Point out each Plasmodium parasite.
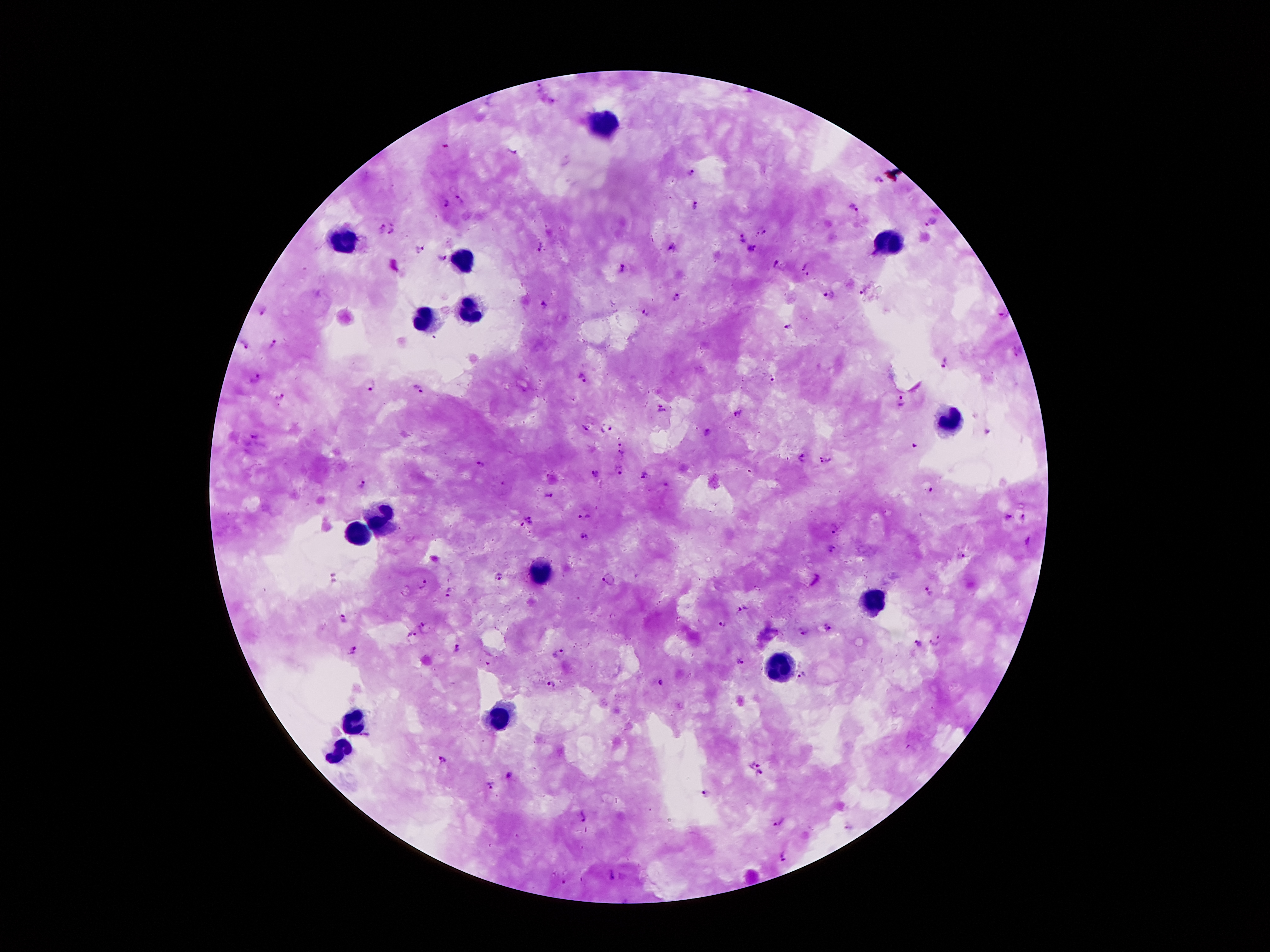

Approximate centers as {x, y} in pixels.
Plasmodium parasites: {540, 87}, {552, 101}, {693, 173}, {878, 180}, {461, 198}, {446, 203}, {696, 207}, {854, 207}, {382, 227}, {764, 232}, {393, 233}, {741, 238}, {539, 246}, {671, 247}, {751, 248}, {418, 250}, {441, 258}, {775, 263}, {805, 266}, {621, 269}, {806, 276}, {861, 291}, {677, 297}, {828, 297}, {545, 305}, {263, 310}, {646, 313}, {791, 328}, {274, 344}, {242, 347}, {941, 363}, {581, 378}, {256, 379}, {775, 380}, {371, 387}, {417, 389}, {280, 397}, {901, 401}, {661, 407}, {740, 413}, {586, 427}, {609, 429}, {708, 431}, {256, 436}, {621, 444}, {623, 455}, {802, 457}, {826, 460}, {479, 464}, {619, 469}, {595, 474}, {645, 476}, {363, 485}, {929, 491}, {545, 496}, {1007, 516}, {584, 518}, {1023, 518}, {526, 522}, {836, 529}, {584, 537}, {1029, 543}, {831, 548}, {962, 557}, {497, 577}, {610, 580}, {422, 583}, {928, 590}, {450, 593}, {741, 608}, {344, 618}, {424, 624}, {722, 624}, {829, 628}, {804, 630}, {411, 637}, {935, 642}, {917, 644}, {353, 649}, {459, 649}, {560, 652}, {738, 662}, {803, 677}, {663, 684}, {553, 685}, {442, 761}, {752, 767}, {761, 774}, {509, 775}, {491, 785}, {705, 794}, {582, 816}, {780, 823}, {783, 857}, {612, 876}.

Summary:
  - Leukocyte locations: {607, 123}, {890, 241}, {346, 243}, {464, 262}, {468, 310}, {428, 321}, {947, 421}, {382, 516}, {359, 533}, {543, 577}, {871, 603}, {783, 668}, {495, 719}, {354, 721}, {342, 750}
  - Field of view: one from this slide
  - Stain: Giemsa
  - Preparation: thick peripheral-blood smear
  - Image size: 1270×952 pixels
  - Capture: smartphone through the microscope eyepiece
  - Patient malaria status: infected with Plasmodium falciparum
  - Magnification: 100x